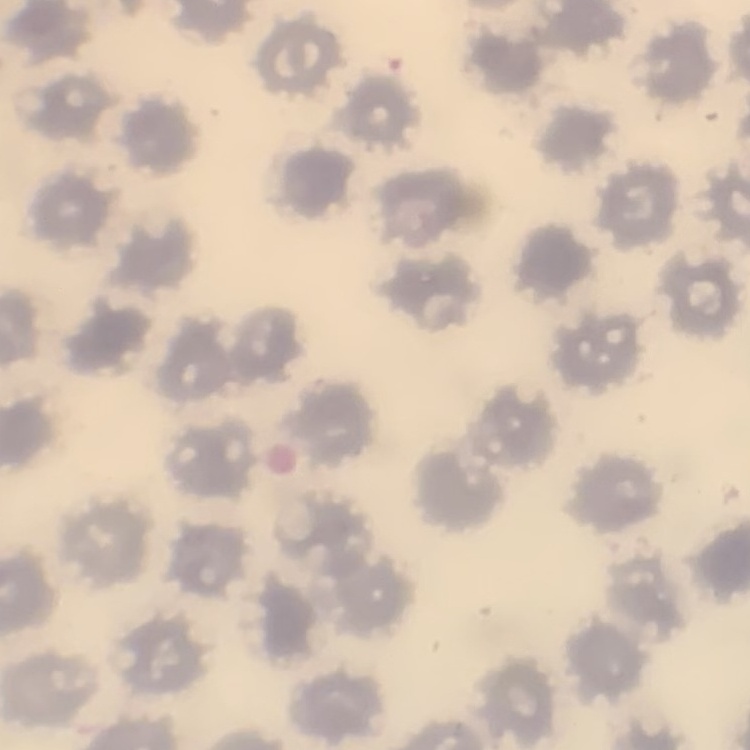

erythrocyte morphology = no rouleaux formation
image type = square crop of a larger photomicrograph
preparation = thin blood smear
stain = Field's or Giemsa